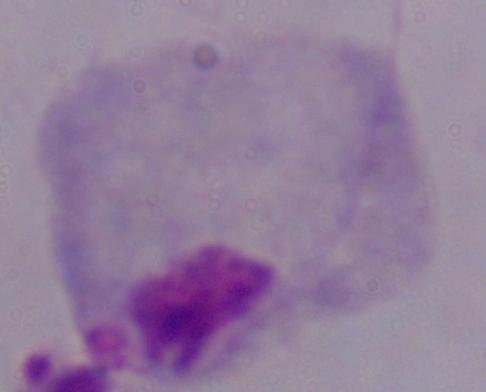

Summary:
  - Modality: micrograph
  - Magnification: 1000x
  - Identification: trichomonad